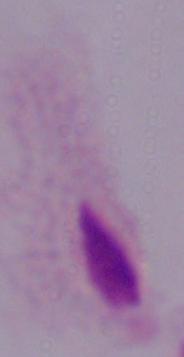
Summary:
  - Modality: photomicrograph
  - Identification: trichomonad
  - Magnification: 1000x